Point out each leukocyte.
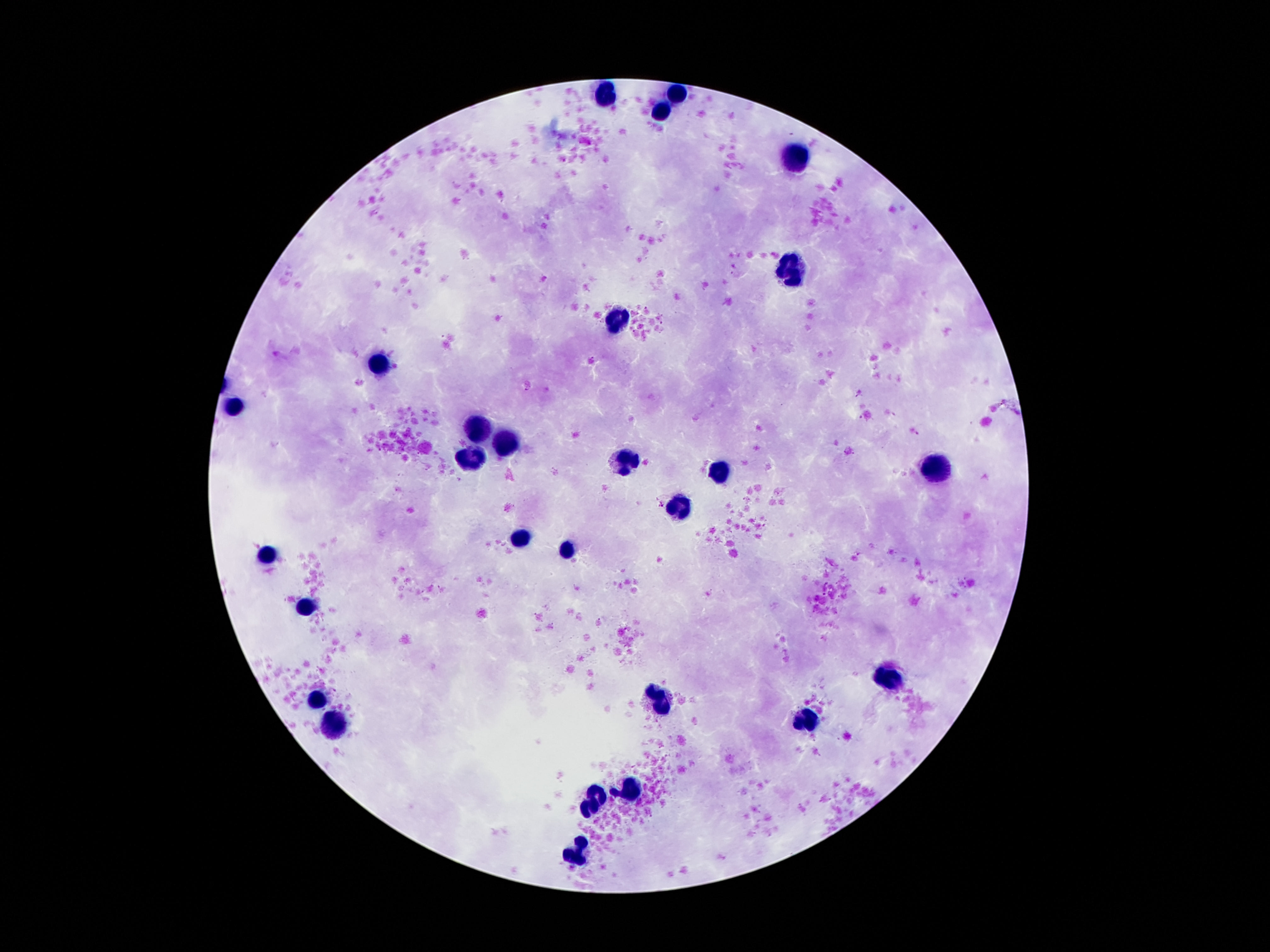

Approximate centers as [x, y] in pixels.
Leukocytes: [679, 93], [607, 94], [658, 112], [801, 160], [788, 267], [620, 318], [381, 365], [236, 404], [480, 425], [506, 440], [625, 462], [470, 465], [722, 471], [938, 471], [676, 506], [518, 537], [567, 552], [266, 554], [307, 605], [890, 678], [661, 699], [316, 701], [806, 719], [334, 723], [628, 790], [597, 794], [590, 803], [584, 840], [573, 858].

capture = smartphone camera through the microscope eyepiece
stain = Giemsa
magnification = 100x
patient malaria status = not infected
preparation = thick blood film
image size = 1270×952 pixels
field of view = one from this slide